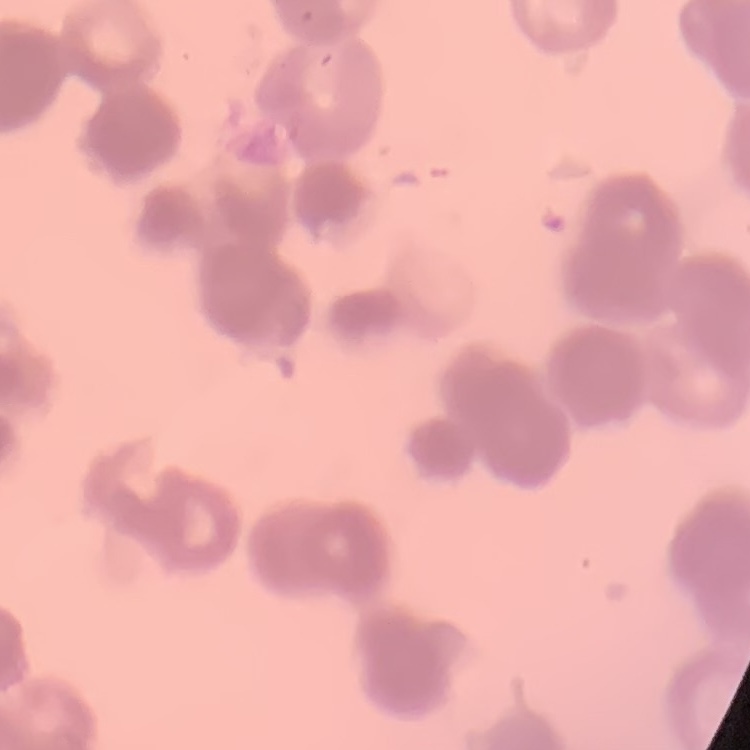

red blood cell morphology = rouleaux formation
image type = square crop of a larger photomicrograph
stain = Field's or Giemsa
preparation = thin blood smear